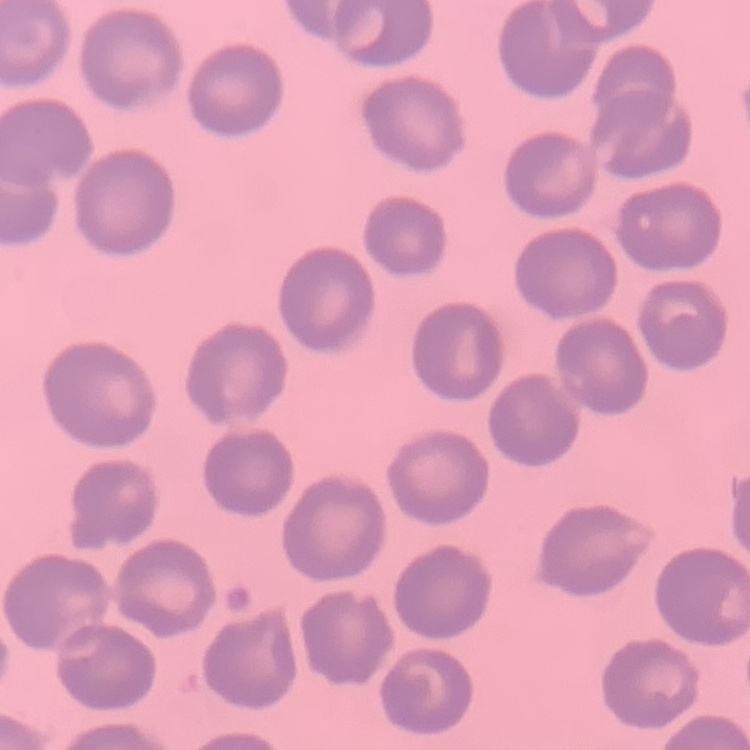

The erythrocytes exhibit no rouleaux formation. Field's or Giemsa stain. One tile cut from a larger photomicrograph. Thin blood film.